Outline each blood parasite and name the species.
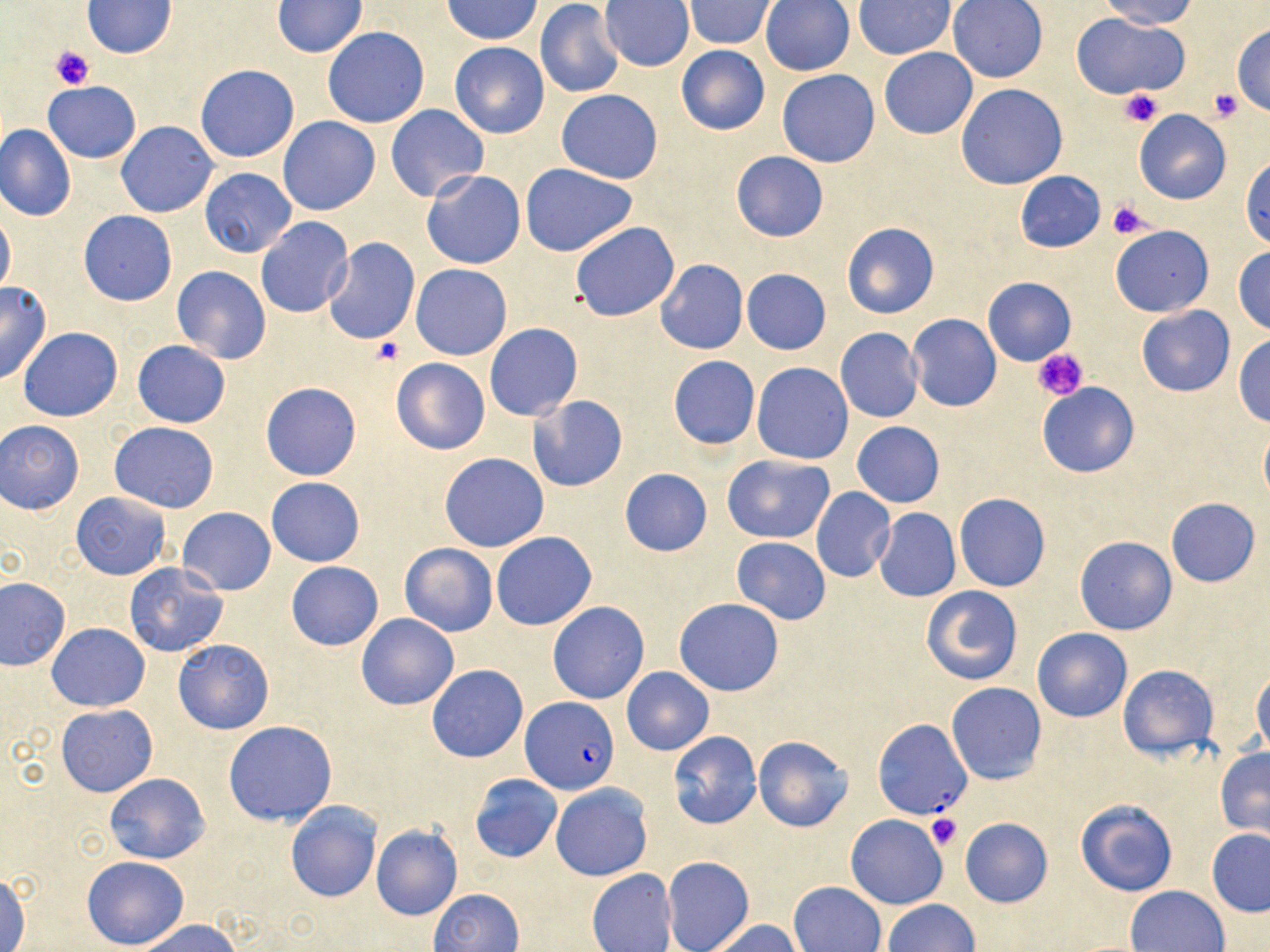
Approximate bounding boxes as named x1/y1/x2/y2 corners in pixels.
Plasmodium falciparum-infected red blood cells: (x1=521, y1=696, x2=619, y2=795), (x1=871, y1=719, x2=972, y2=821).
No Plasmodium ovale, Plasmodium malariae, Plasmodium vivax, Babesia divergens, or Trypanosoma brucei observed.

slide_level_diagnosis: Plasmodium falciparum
modality: light microscopy
preparation: thin blood smear
platelet_locations: 'approximate bounding boxes as named x1/y1/x2/y2 corners in pixels: (x1=50, y1=46, x2=94, y2=91), (x1=1119, y1=88, x2=1163, y2=128), (x1=1207, y1=88, x2=1244, y2=122), (x1=1107, y1=199, x2=1155, y2=240), (x1=369, y1=338, x2=404, y2=367), (x1=1034, y1=348, x2=1089, y2=403), (x1=925, y1=813, x2=961, y2=851)'
image_size: 1270×952 pixels
uninfected_red_blood_cell_locations: 'approximate bounding boxes as named x1/y1/x2/y2 corners in pixels: (x1=443, y1=0, x2=544, y2=43), (x1=947, y1=0, x2=1048, y2=83), (x1=1098, y1=0, x2=1199, y2=28), (x1=82, y1=1, x2=178, y2=58), (x1=272, y1=1, x2=367, y2=57), (x1=683, y1=1, x2=779, y2=49), (x1=759, y1=1, x2=855, y2=76), (x1=854, y1=1, x2=957, y2=60), (x1=535, y1=2, x2=626, y2=100), (x1=599, y1=2, x2=695, y2=71), (x1=1073, y1=14, x2=1189, y2=99), (x1=1231, y1=23, x2=1270, y2=114), (x1=322, y1=27, x2=430, y2=127), (x1=449, y1=41, x2=549, y2=139), (x1=675, y1=45, x2=771, y2=136), (x1=878, y1=48, x2=978, y2=139), (x1=196, y1=64, x2=300, y2=162), (x1=778, y1=70, x2=879, y2=168), (x1=42, y1=81, x2=141, y2=163), (x1=955, y1=84, x2=1067, y2=189), (x1=556, y1=89, x2=663, y2=184), (x1=386, y1=104, x2=488, y2=202), (x1=1133, y1=110, x2=1232, y2=204), (x1=278, y1=116, x2=379, y2=215), (x1=116, y1=122, x2=218, y2=218), (x1=0, y1=123, x2=76, y2=222), (x1=731, y1=151, x2=829, y2=242), (x1=1241, y1=157, x2=1270, y2=249), (x1=520, y1=164, x2=639, y2=258), (x1=200, y1=168, x2=296, y2=257), (x1=420, y1=169, x2=526, y2=270), (x1=1015, y1=171, x2=1105, y2=252), (x1=0, y1=208, x2=15, y2=298), (x1=78, y1=210, x2=177, y2=305), (x1=256, y1=216, x2=354, y2=319), (x1=570, y1=221, x2=680, y2=323), (x1=841, y1=222, x2=938, y2=319), (x1=1111, y1=226, x2=1213, y2=315), (x1=324, y1=239, x2=419, y2=345), (x1=1232, y1=246, x2=1270, y2=336), (x1=656, y1=259, x2=748, y2=354), (x1=411, y1=264, x2=512, y2=360), (x1=171, y1=266, x2=272, y2=364), (x1=741, y1=269, x2=831, y2=354), (x1=983, y1=277, x2=1076, y2=365), (x1=0, y1=282, x2=52, y2=385), (x1=1137, y1=305, x2=1235, y2=397), (x1=907, y1=313, x2=1001, y2=412), (x1=484, y1=323, x2=582, y2=422), (x1=18, y1=327, x2=123, y2=422), (x1=835, y1=328, x2=924, y2=424), (x1=1233, y1=335, x2=1270, y2=427), (x1=132, y1=340, x2=231, y2=428), (x1=667, y1=355, x2=761, y2=449), (x1=391, y1=358, x2=489, y2=455), (x1=752, y1=362, x2=854, y2=465), (x1=261, y1=382, x2=362, y2=480), (x1=1037, y1=383, x2=1139, y2=477), (x1=529, y1=395, x2=628, y2=491), (x1=1, y1=420, x2=85, y2=514), (x1=110, y1=421, x2=219, y2=512), (x1=852, y1=421, x2=945, y2=508), (x1=1260, y1=421, x2=1270, y2=507), (x1=439, y1=453, x2=549, y2=552), (x1=723, y1=454, x2=835, y2=544), (x1=618, y1=467, x2=713, y2=556), (x1=267, y1=477, x2=364, y2=566), (x1=810, y1=487, x2=895, y2=583), (x1=72, y1=491, x2=170, y2=580), (x1=954, y1=493, x2=1050, y2=591), (x1=1166, y1=497, x2=1260, y2=587), (x1=178, y1=507, x2=276, y2=595), (x1=874, y1=508, x2=961, y2=602), (x1=491, y1=532, x2=597, y2=631), (x1=1075, y1=536, x2=1177, y2=636), (x1=730, y1=538, x2=832, y2=624), (x1=400, y1=543, x2=497, y2=637), (x1=124, y1=562, x2=230, y2=657), (x1=286, y1=562, x2=383, y2=650), (x1=0, y1=577, x2=70, y2=668), (x1=921, y1=586, x2=1023, y2=685), (x1=674, y1=598, x2=785, y2=696), (x1=547, y1=601, x2=650, y2=704), (x1=356, y1=612, x2=459, y2=710), (x1=47, y1=623, x2=149, y2=712), (x1=1032, y1=627, x2=1132, y2=722), (x1=173, y1=637, x2=274, y2=735), (x1=427, y1=665, x2=528, y2=763), (x1=1118, y1=665, x2=1217, y2=760), (x1=622, y1=667, x2=713, y2=755), (x1=1251, y1=670, x2=1270, y2=759), (x1=947, y1=682, x2=1046, y2=784), (x1=57, y1=704, x2=158, y2=797), (x1=224, y1=720, x2=337, y2=826), (x1=669, y1=731, x2=761, y2=829), (x1=754, y1=735, x2=853, y2=831), (x1=1215, y1=748, x2=1270, y2=837), (x1=104, y1=773, x2=210, y2=865), (x1=470, y1=773, x2=562, y2=863), (x1=550, y1=782, x2=652, y2=882), (x1=1076, y1=799, x2=1178, y2=896), (x1=285, y1=802, x2=382, y2=903), (x1=845, y1=812, x2=948, y2=910), (x1=959, y1=816, x2=1052, y2=908), (x1=371, y1=825, x2=462, y2=921), (x1=1206, y1=828, x2=1270, y2=917), (x1=81, y1=856, x2=189, y2=949), (x1=662, y1=856, x2=753, y2=952), (x1=587, y1=868, x2=677, y2=952), (x1=0, y1=872, x2=31, y2=952), (x1=789, y1=881, x2=886, y2=952), (x1=1126, y1=885, x2=1230, y2=951), (x1=428, y1=888, x2=523, y2=951), (x1=883, y1=899, x2=978, y2=951), (x1=133, y1=919, x2=242, y2=952), (x1=707, y1=919, x2=805, y2=952)'
magnification: 1000x
stain: May-Grünwald-Giemsa
field_of_view: single